Locate every Plasmodium vivax-infected red blood cell.
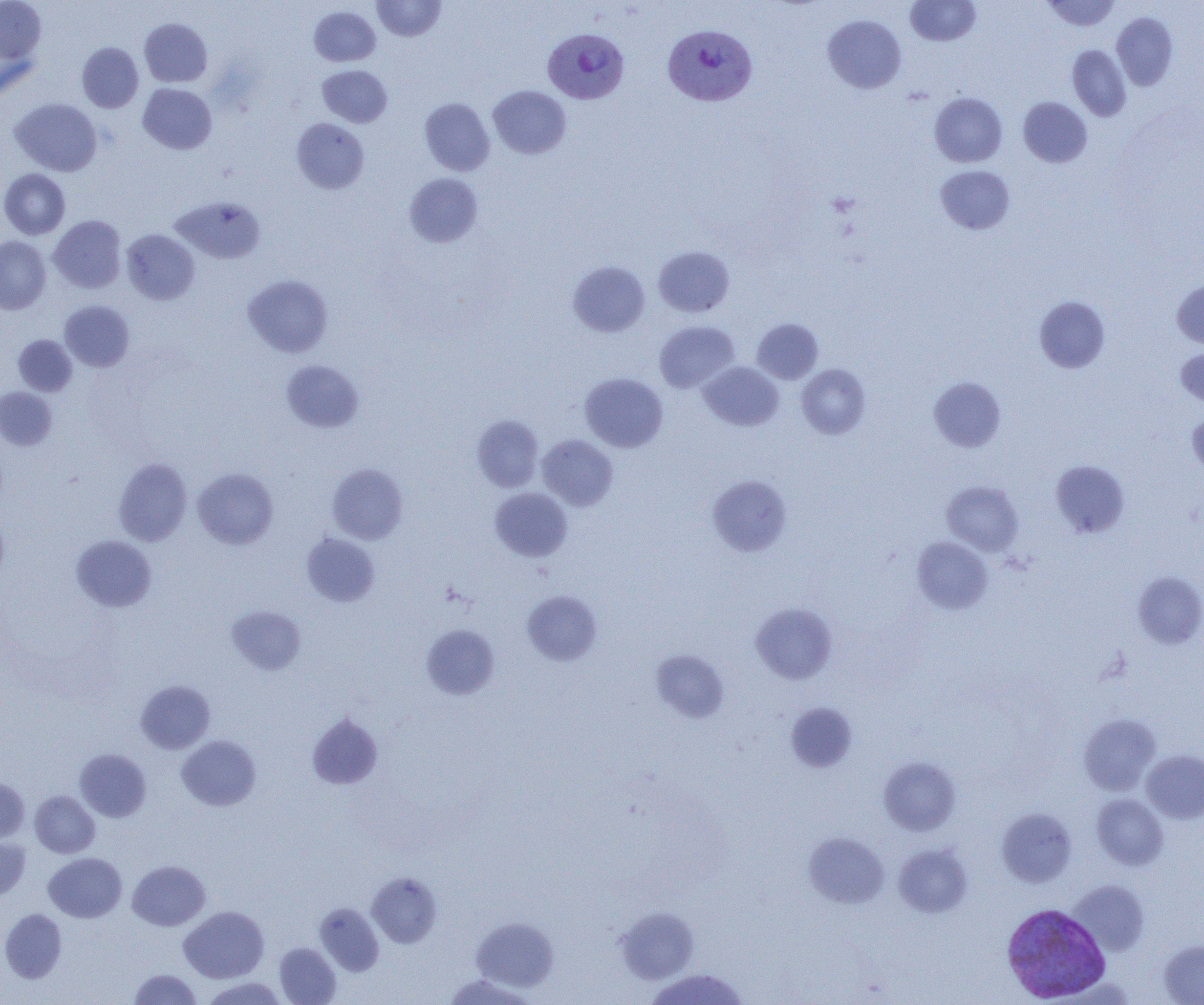
Approximate bounding boxes as (x1, y1, x2, y2) in pixels.
Plasmodium vivax-infected red blood cells: (662, 24, 758, 105), (542, 29, 629, 104), (1002, 903, 1111, 1002).

Summary:
  - Uninfected red blood cell locations: (0, 0, 46, 63), (372, 0, 446, 41), (905, 0, 980, 46), (1042, 0, 1121, 31), (309, 6, 381, 66), (1112, 12, 1178, 91), (823, 15, 906, 93), (139, 18, 212, 87), (0, 40, 39, 105), (77, 42, 143, 113), (1067, 45, 1131, 122), (317, 65, 392, 127), (138, 83, 216, 154), (488, 85, 571, 159), (929, 92, 1007, 167), (420, 97, 495, 176), (1018, 97, 1092, 167), (10, 98, 102, 176), (291, 118, 369, 194), (935, 165, 1015, 234), (0, 169, 69, 239), (404, 173, 483, 248), (171, 196, 265, 264), (48, 215, 126, 293), (121, 229, 199, 304), (0, 237, 50, 314), (653, 246, 734, 317), (567, 261, 650, 337), (243, 274, 333, 357), (1172, 280, 1204, 348), (1034, 296, 1110, 373), (59, 301, 134, 371), (751, 318, 823, 384), (654, 320, 740, 393), (13, 335, 77, 396), (1176, 348, 1204, 409), (281, 360, 364, 433), (699, 361, 783, 431), (797, 364, 871, 439), (580, 373, 667, 452), (928, 377, 1006, 452), (0, 387, 57, 451), (1186, 410, 1204, 476), (472, 414, 544, 492), (537, 435, 618, 510), (114, 458, 191, 545), (1050, 460, 1130, 538), (327, 464, 408, 544), (193, 468, 277, 549), (708, 475, 791, 556), (942, 481, 1024, 555), (490, 488, 572, 561), (0, 511, 9, 585), (301, 532, 380, 606), (71, 535, 157, 612), (912, 536, 994, 614), (1134, 572, 1204, 648), (522, 590, 602, 665), (750, 603, 837, 684), (227, 605, 306, 674), (421, 624, 499, 700), (651, 650, 729, 723), (136, 680, 215, 753), (785, 702, 857, 773), (307, 712, 383, 790), (1079, 713, 1161, 795), (177, 735, 261, 810), (75, 749, 151, 822), (1141, 750, 1204, 823), (879, 757, 961, 835), (0, 778, 29, 843), (30, 790, 100, 858), (1091, 794, 1168, 870), (996, 807, 1076, 887), (804, 832, 889, 908), (0, 838, 30, 900), (893, 843, 972, 917), (44, 853, 126, 922), (127, 860, 209, 930), (367, 872, 442, 948), (1068, 879, 1149, 956), (315, 903, 384, 976), (179, 906, 269, 983), (615, 906, 699, 984), (0, 908, 67, 983), (471, 917, 559, 991), (1158, 939, 1204, 1004), (274, 943, 340, 1004), (644, 968, 750, 1005), (129, 969, 202, 1004), (444, 974, 535, 1005), (201, 977, 287, 1005)
  - Slide-level diagnosis: Plasmodium vivax
  - Field of view: single
  - Modality: optical microscopy
  - Magnification: 1000x
  - Preparation: thin blood smear
  - Image size: 1204×1005 pixels